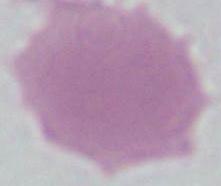
identification = red blood cell
modality = micrograph
magnification = 1000x